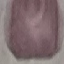
result = no malaria parasites detected
image type = cell patch, automatically extracted from a larger field of view and resized to 64 × 64 pixels
preparation = thin blood film
capture = smartphone through the microscope eyepiece
stain = Giemsa